Describe the morphology of the erythrocytes.
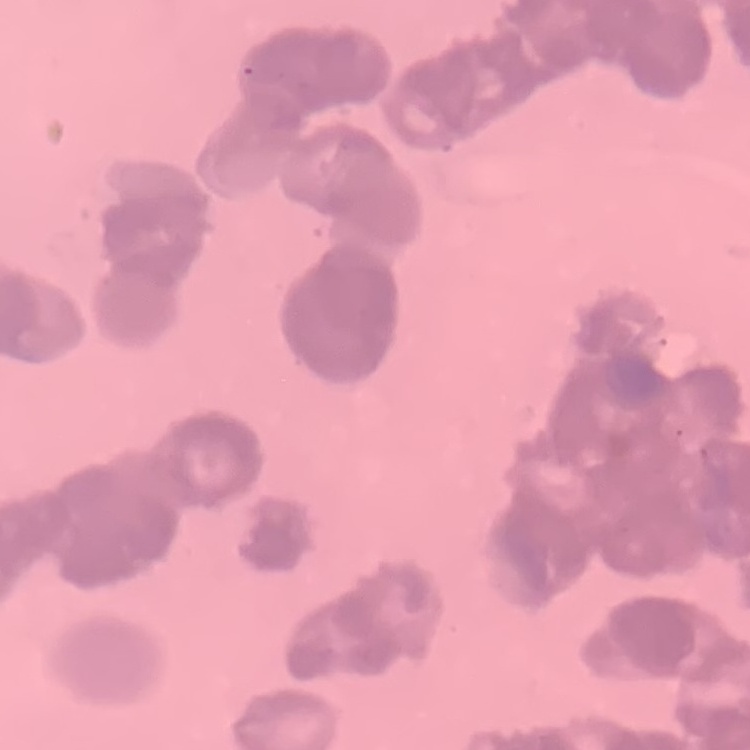

Rouleaux formation.

stain = Field's or Giemsa
preparation = thin blood smear
image type = square crop of a larger photomicrograph